Identify the preparation type.
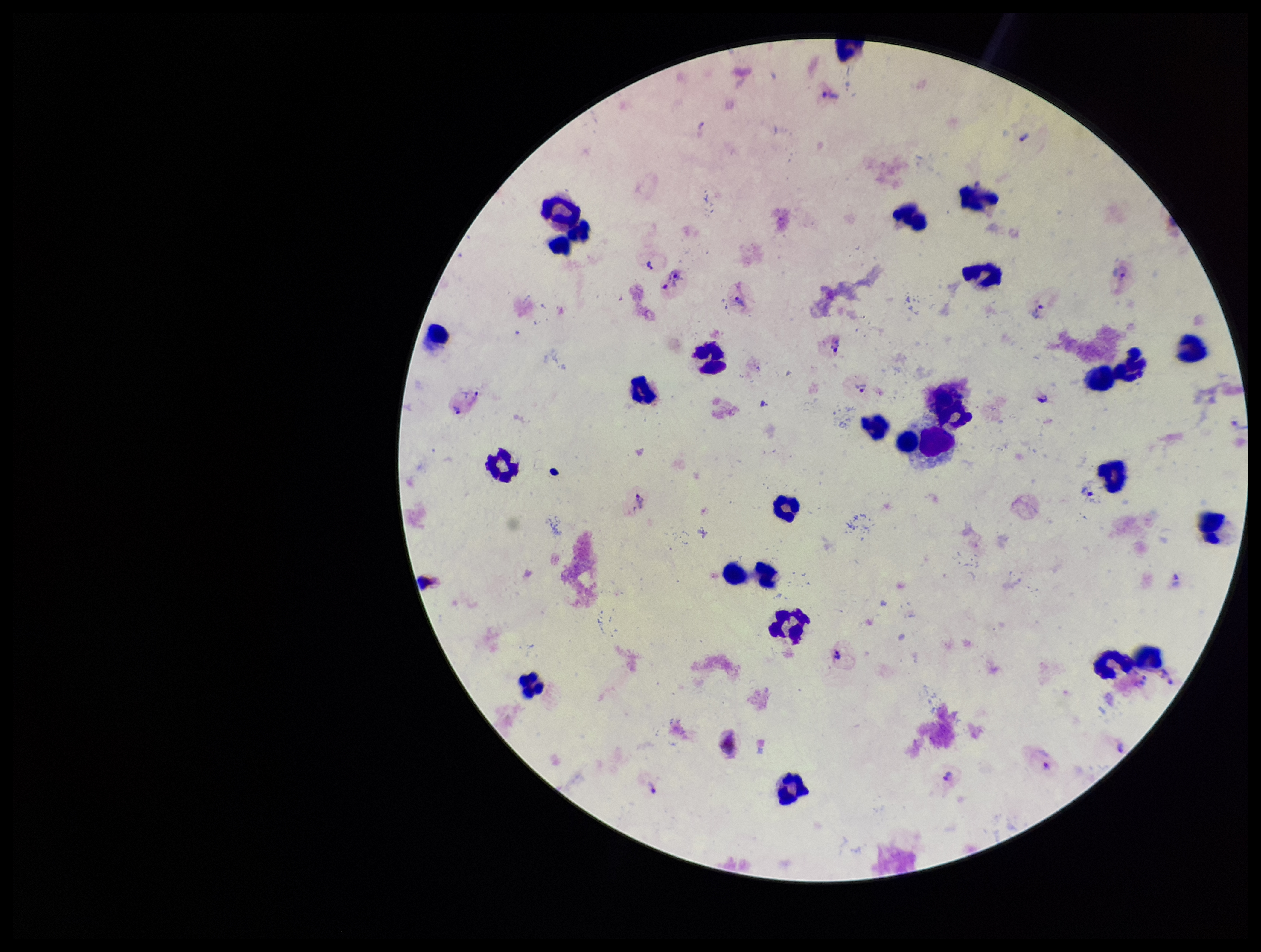

It is a thick blood smear.

Summary:
  - Parasite count: 17
  - Species reported for this patient: Plasmodium vivax
  - Plasmodium parasites: identified
  - Patient malaria status: positive
  - Image size: 1261×952 pixels
  - Leukocyte count: 27
  - Field of view: single
  - Stain: Giemsa
  - Capture: smartphone photograph through the microscope eyepiece